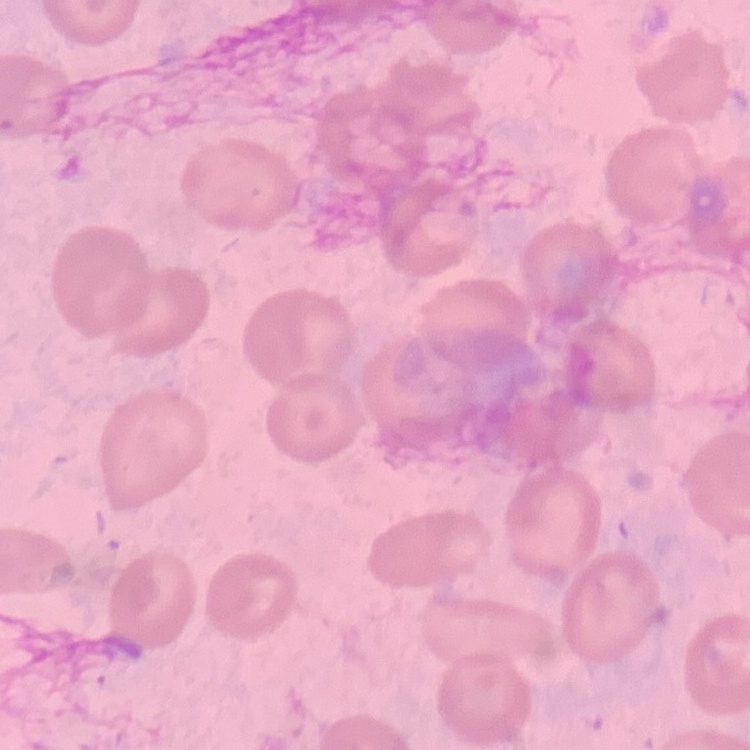
red_blood_cell_morphology: no rouleaux formation
image_type: square crop of a larger photomicrograph
preparation: thin peripheral smear
stain: Field's or Giemsa